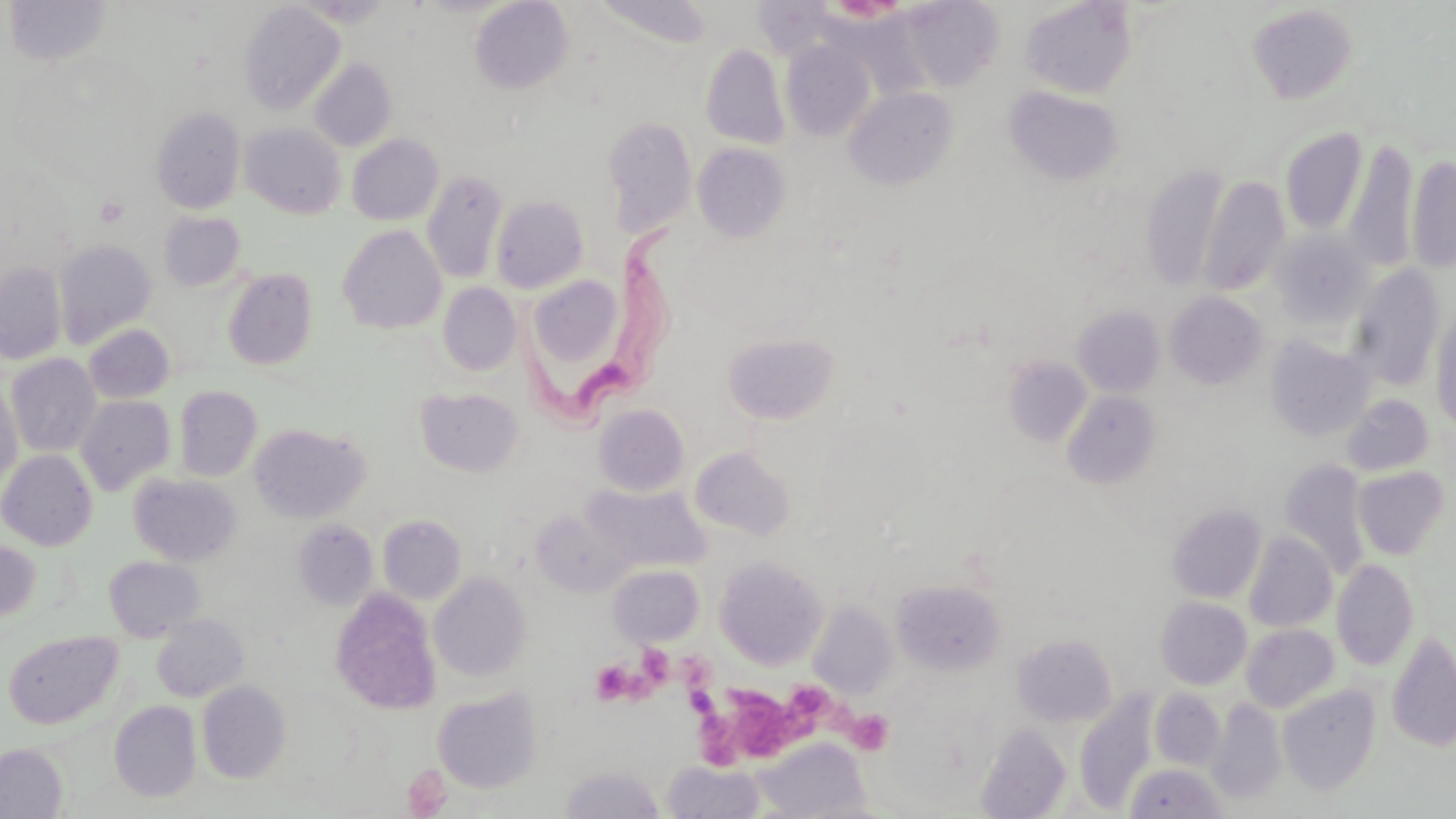

Approximate bounding boxes as (x1,y1)-(x2,y2) corner pairs in pixels. Uninfected red blood cell locations: (291,0)-(396,26), (1020,0)-(1137,98), (3,1)-(112,67), (239,1)-(346,116), (470,1)-(574,94), (754,1)-(838,59), (902,2)-(1003,90), (1247,4)-(1359,104), (781,38)-(876,141), (701,44)-(789,148), (309,58)-(397,152), (845,86)-(958,189), (1004,86)-(1124,186), (151,106)-(246,214), (602,117)-(698,235), (240,122)-(345,219), (1280,127)-(1370,236), (347,134)-(443,225), (1343,138)-(1420,271), (693,143)-(791,242), (1406,156)-(1456,273), (1140,162)-(1229,291), (421,169)-(508,283), (1198,176)-(1290,298), (492,196)-(588,293), (159,211)-(246,291), (338,225)-(447,334), (1268,228)-(1375,331), (53,239)-(156,348), (0,262)-(67,364), (1347,265)-(1446,392), (223,267)-(318,370), (525,275)-(627,370), (438,282)-(522,376), (1165,292)-(1268,390), (1430,304)-(1456,434), (1073,305)-(1165,397), (84,324)-(175,403), (722,333)-(839,424), (1265,335)-(1375,441), (6,354)-(101,457), (1004,358)-(1093,447), (0,378)-(22,491), (174,386)-(262,482), (415,387)-(524,477), (1063,390)-(1160,488), (1342,394)-(1434,476), (76,395)-(175,495), (594,404)-(690,496), (249,423)-(369,523), (690,447)-(796,541), (0,450)-(98,550), (1279,459)-(1371,581), (1353,466)-(1450,560), (130,474)-(242,566), (583,482)-(710,572), (1166,503)-(1266,604), (530,507)-(635,598), (378,515)-(467,604), (293,519)-(379,611), (1244,531)-(1338,632), (0,541)-(40,625), (715,555)-(828,670), (104,556)-(204,642), (1332,559)-(1418,670), (608,565)-(704,647), (430,572)-(532,683), (892,577)-(1005,676), (331,588)-(441,715), (1156,597)-(1252,689), (808,600)-(897,700), (152,614)-(248,702), (1241,624)-(1339,713), (3,630)-(122,729), (1386,632)-(1456,752), (1012,634)-(1117,727), (197,680)-(291,783), (1278,685)-(1380,795), (432,687)-(542,794), (1150,688)-(1226,771), (1074,691)-(1159,813), (1207,698)-(1286,804), (110,701)-(201,802), (976,722)-(1071,818), (753,738)-(871,818), (0,743)-(68,818), (662,760)-(767,819), (1125,763)-(1227,819), (559,764)-(666,818). Platelet locations: (95,196)-(129,227), (634,645)-(676,691), (676,651)-(719,695), (589,661)-(632,705), (783,679)-(834,739), (720,682)-(799,766), (688,688)-(727,723), (697,710)-(744,765), (847,710)-(894,755), (403,765)-(452,816). Trypanosoma brucei locations: (511,212)-(698,431). Slide-level diagnosis: Trypanosoma brucei. Thin blood film. Optical microscopy. One field of a larger specimen. 1000x magnification. May-Grünwald-Giemsa-stained preparation. Image is 1456×819 pixels.